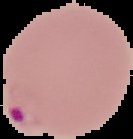 Segmented cell region on a black background. From a thin blood smear. Image is 133×139 pixels. Malaria status: parasitized.